Report the malaria status of this cell.
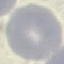

Uninfected.

Giemsa stain. Automatically extracted cell patch, resized to 64 × 64 pixels. Thin blood smear. Acquired by smartphone through the microscope eyepiece.